Assess for malaria.
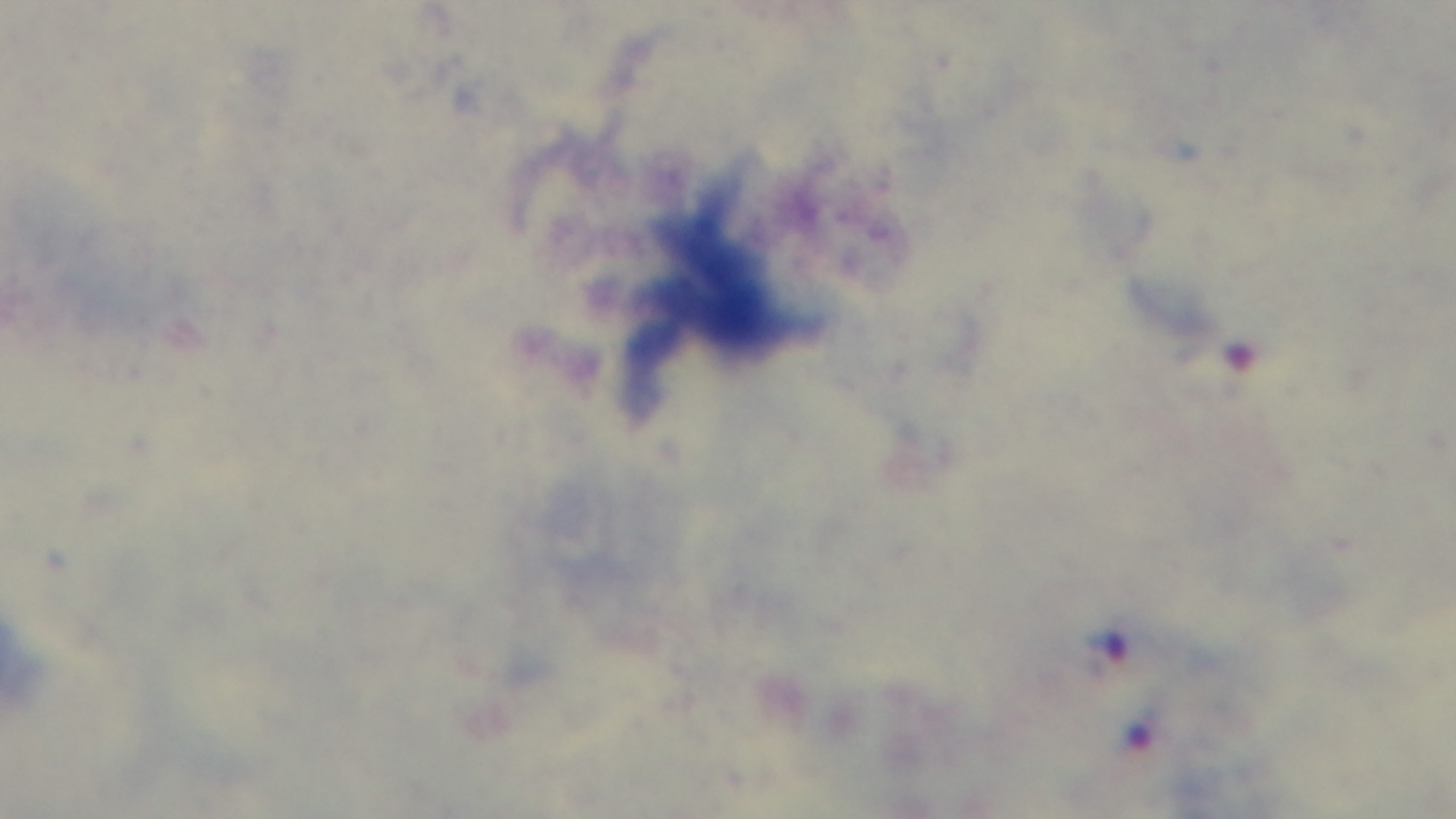
Infected.

field of view = one from the slide
objective = 100x oil immersion
modality = light microscopy
stain = Giemsa
capture = mounted 4K digital camera
preparation = thick